Describe the morphology of the erythrocytes.
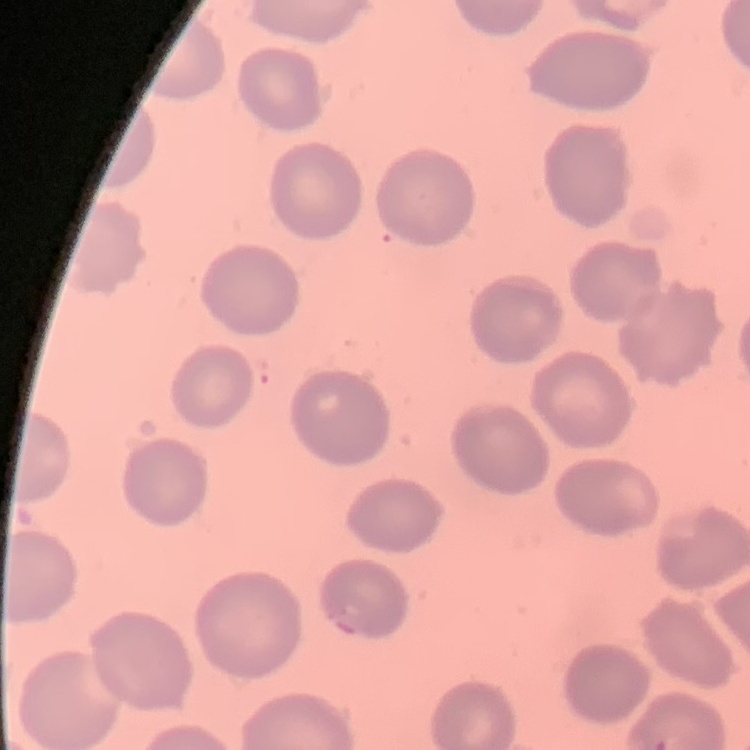

They show no rouleaux formation.

Summary:
  - Image type: one tile cut from a larger photomicrograph
  - Preparation: thin peripheral smear
  - Stain: Field's or Giemsa